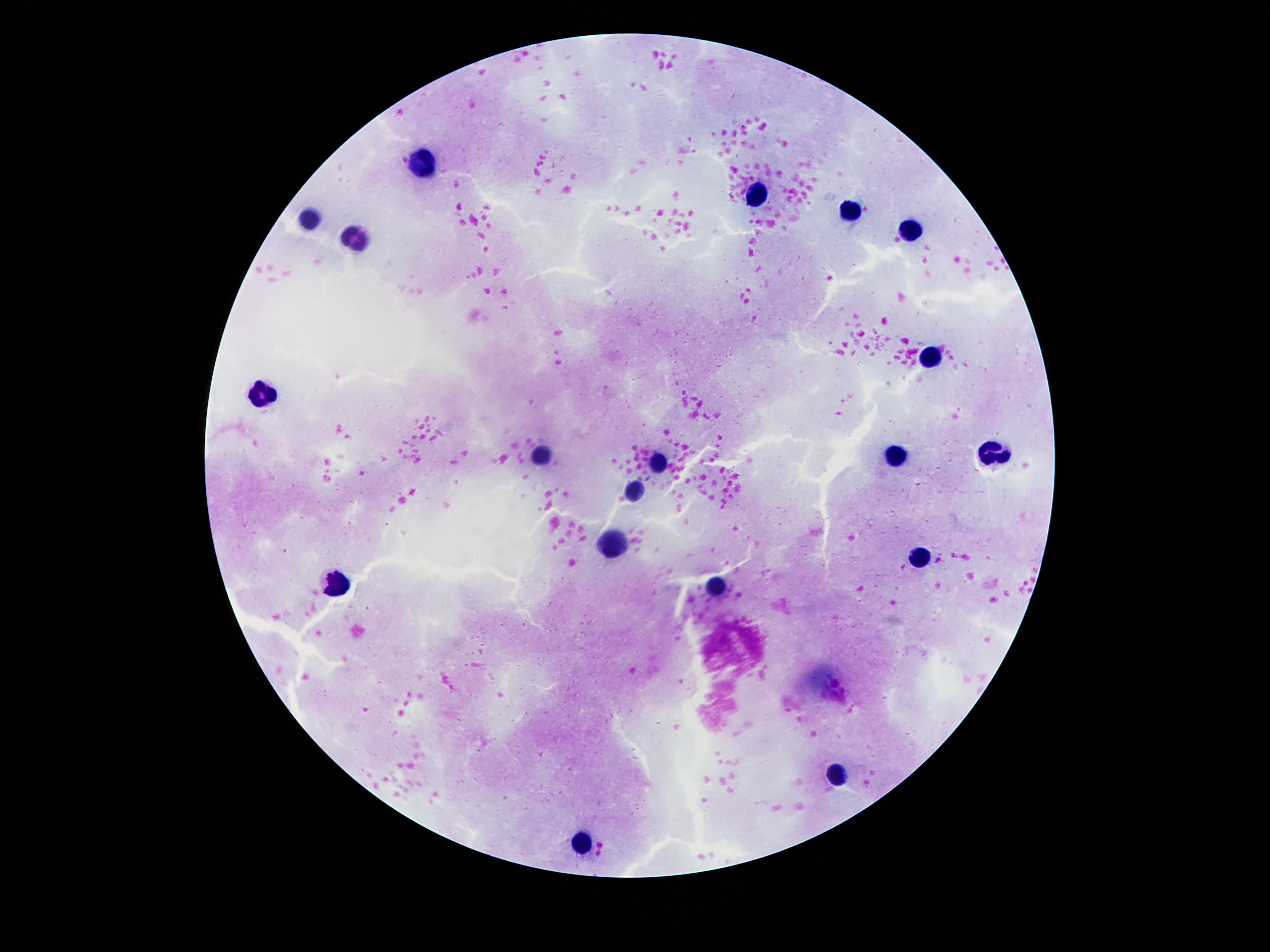

image size = 1270×952 pixels
field of view = one from this slide
magnification = 100x
stain = Giemsa
capture = smartphone camera through the microscope eyepiece
preparation = thick blood smear
patient malaria status = uninfected
leukocyte locations = approximate object centers, in pixels from the top-left corner: (x=424, y=159), (x=753, y=191), (x=844, y=212), (x=307, y=219), (x=912, y=233), (x=354, y=240), (x=931, y=356), (x=263, y=394), (x=898, y=457), (x=991, y=457), (x=543, y=459), (x=658, y=462), (x=634, y=488), (x=609, y=544), (x=919, y=558), (x=718, y=583), (x=340, y=585), (x=837, y=772), (x=583, y=842)